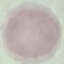
Malaria status: uninfected. Thin blood film. Automatically extracted cell patch, resized to 64 × 64 pixels. Giemsa-stained preparation. Acquired by smartphone through the microscope eyepiece.